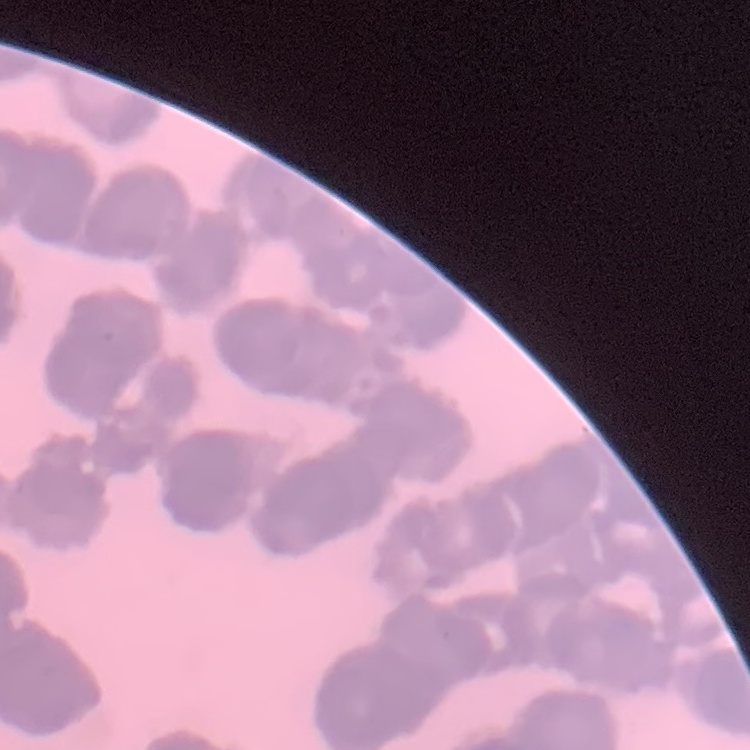
The erythrocytes exhibit rouleaux formation. Stained with either Field's or Giemsa. Thin peripheral smear. Square crop of a larger photomicrograph.